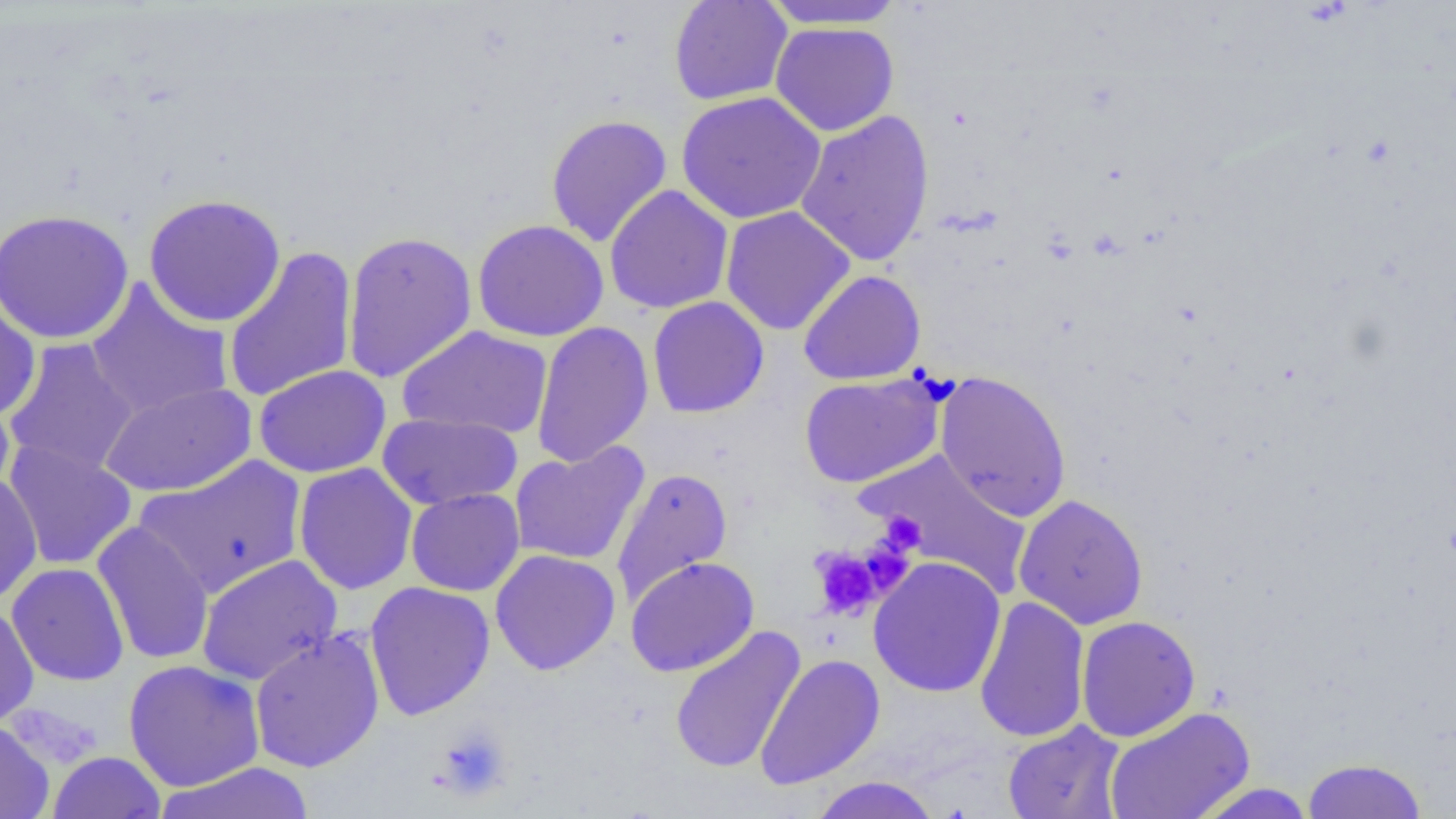 Approximate bounding boxes as named x1/y1/x2/y2 corners in pixels. Uninfected red blood cell locations: (x1=668, y1=0, x2=794, y2=106), (x1=760, y1=0, x2=909, y2=31), (x1=770, y1=22, x2=899, y2=136), (x1=676, y1=92, x2=826, y2=224), (x1=795, y1=109, x2=935, y2=268), (x1=545, y1=114, x2=673, y2=247), (x1=604, y1=184, x2=734, y2=314), (x1=143, y1=193, x2=286, y2=327), (x1=720, y1=206, x2=856, y2=335), (x1=0, y1=209, x2=134, y2=345), (x1=472, y1=219, x2=609, y2=342), (x1=341, y1=230, x2=478, y2=384), (x1=222, y1=245, x2=359, y2=405), (x1=798, y1=269, x2=927, y2=385), (x1=85, y1=279, x2=234, y2=420), (x1=647, y1=296, x2=769, y2=419), (x1=0, y1=297, x2=41, y2=422), (x1=531, y1=320, x2=654, y2=468), (x1=397, y1=325, x2=553, y2=439), (x1=2, y1=338, x2=141, y2=478), (x1=253, y1=364, x2=391, y2=479), (x1=933, y1=370, x2=1072, y2=523), (x1=798, y1=372, x2=947, y2=488), (x1=99, y1=381, x2=257, y2=498), (x1=0, y1=385, x2=15, y2=499), (x1=377, y1=413, x2=522, y2=510), (x1=3, y1=440, x2=138, y2=570), (x1=509, y1=441, x2=650, y2=567), (x1=859, y1=448, x2=1034, y2=597), (x1=135, y1=455, x2=308, y2=599), (x1=293, y1=463, x2=418, y2=595), (x1=611, y1=467, x2=733, y2=607), (x1=0, y1=473, x2=42, y2=605), (x1=405, y1=488, x2=525, y2=597), (x1=1013, y1=494, x2=1149, y2=630), (x1=92, y1=521, x2=214, y2=665), (x1=489, y1=549, x2=621, y2=675), (x1=196, y1=553, x2=343, y2=686), (x1=625, y1=556, x2=759, y2=677), (x1=868, y1=557, x2=1007, y2=698), (x1=7, y1=563, x2=130, y2=686), (x1=364, y1=580, x2=496, y2=720), (x1=974, y1=594, x2=1090, y2=744), (x1=0, y1=604, x2=39, y2=728), (x1=1075, y1=615, x2=1201, y2=742), (x1=668, y1=625, x2=806, y2=775), (x1=249, y1=628, x2=385, y2=773), (x1=754, y1=653, x2=886, y2=789), (x1=123, y1=659, x2=266, y2=792), (x1=1103, y1=706, x2=1255, y2=819), (x1=0, y1=720, x2=54, y2=819), (x1=1002, y1=720, x2=1126, y2=819), (x1=49, y1=751, x2=166, y2=818), (x1=1301, y1=757, x2=1427, y2=818), (x1=153, y1=762, x2=316, y2=818), (x1=807, y1=776, x2=943, y2=819), (x1=1190, y1=783, x2=1318, y2=818). Platelet locations: (x1=878, y1=511, x2=925, y2=554), (x1=858, y1=539, x2=915, y2=596), (x1=811, y1=547, x2=885, y2=621), (x1=434, y1=724, x2=512, y2=801). Slide-level diagnosis: no evidence of blood parasites. Image is 1456×819 pixels. Optical microscopy. One field of a larger specimen. 1000x magnification. Thin blood film.